Outline each blood parasite and name the species.
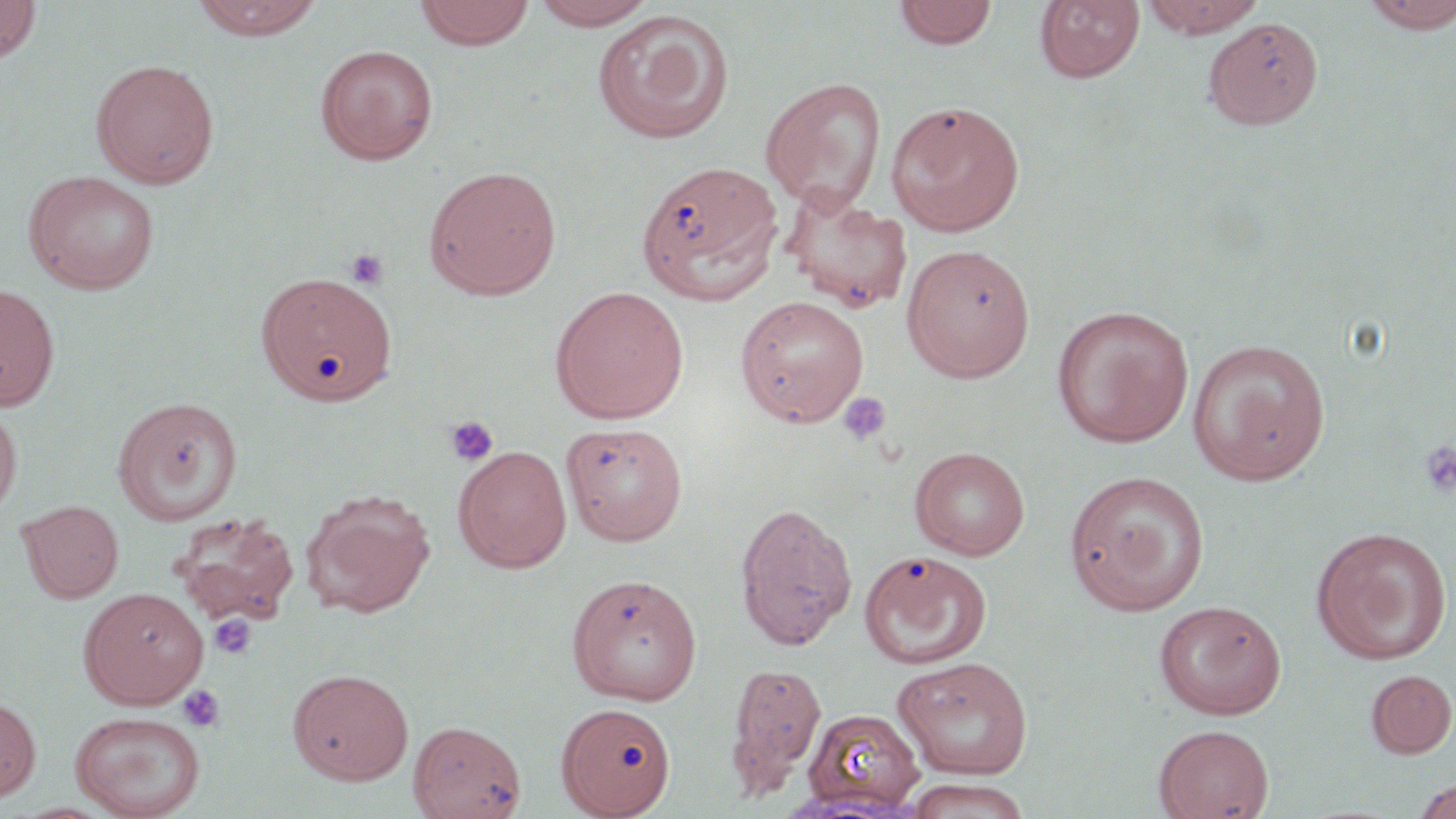

No blood parasites seen.

Approximate bounding boxes as (x1,y1)-(x2,y2) corner pairs in pixels. Uninfected red blood cell locations: (0,0)-(41,64), (189,0)-(323,41), (415,0)-(535,50), (529,0)-(659,30), (1139,0)-(1265,39), (892,1)-(999,51), (1034,1)-(1145,85), (1358,1)-(1456,34), (591,9)-(734,145), (315,44)-(438,164), (90,58)-(220,188), (759,77)-(888,213), (886,101)-(1025,237), (641,162)-(789,309), (424,165)-(562,300), (23,170)-(160,294), (779,184)-(914,314), (900,244)-(1035,383), (256,271)-(398,405), (0,283)-(60,412), (549,285)-(689,423), (735,295)-(869,426), (1051,304)-(1194,448), (1187,338)-(1331,485), (112,396)-(243,525), (0,403)-(22,518), (561,421)-(688,545), (453,445)-(572,573), (909,446)-(1031,560), (1064,469)-(1211,615), (302,489)-(435,618), (17,499)-(124,603), (734,502)-(857,649), (170,512)-(300,627), (1311,525)-(1452,665), (859,550)-(992,670), (566,573)-(703,705), (78,587)-(208,708), (1154,600)-(1287,719), (891,656)-(1034,780), (724,661)-(826,801), (287,667)-(413,784), (1365,668)-(1456,758), (0,697)-(41,802), (558,706)-(678,819), (802,707)-(925,814), (70,711)-(206,818), (408,719)-(526,818), (1153,723)-(1274,819), (901,777)-(1035,819), (1411,777)-(1456,819). Platelet locations: (344,248)-(390,289), (837,391)-(892,447), (445,416)-(500,467), (1418,440)-(1456,498), (210,615)-(257,659), (176,684)-(226,733). Slide-level diagnosis: no evidence of blood parasites. Image is 1456×819 pixels. Light microscopy. May-Grünwald-Giemsa stain. Thin blood film. One field of a larger specimen. 1000x magnification.